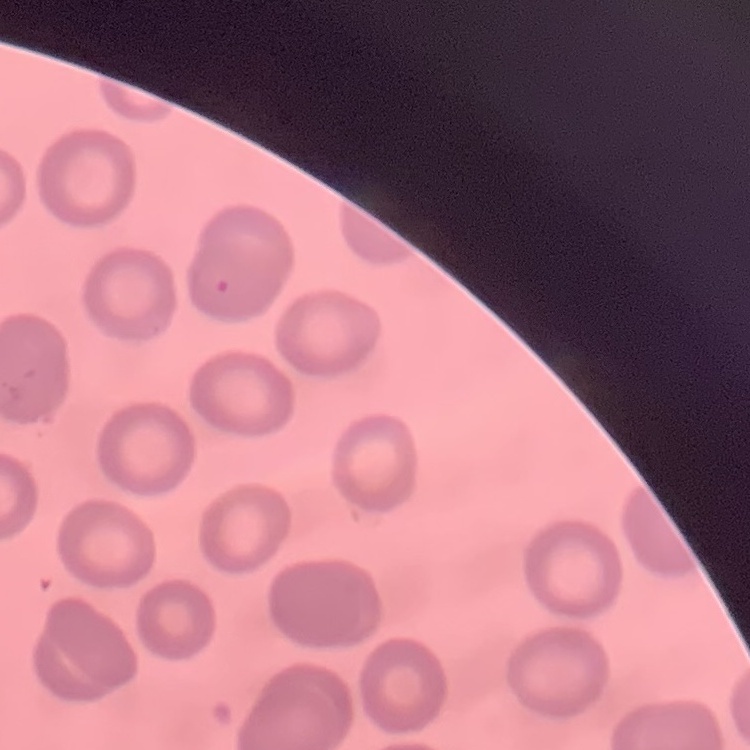

Summary:
  - Erythrocyte morphology: no rouleaux formation
  - Stain: Field's or Giemsa
  - Preparation: thin blood film
  - Image type: one tile cut from a larger photomicrograph